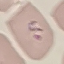
Result: malaria parasites identified. Thin smear of blood. Cell patch, automatically extracted from a larger field of view and resized to 64 × 64 pixels. Giemsa-stained preparation. Acquired by smartphone through the microscope eyepiece.